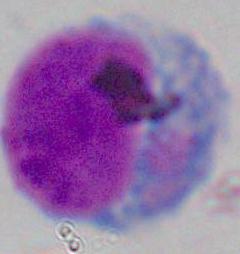

modality = micrograph
magnification = 1000x
identification = leukocyte